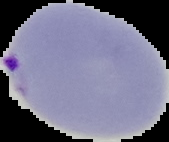
result: Plasmodium parasites detected
preparation: thin blood smear
image_type: segmented cell region with the area outside set to black
image_size: 169×142 pixels